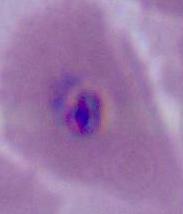

identification: Plasmodium
magnification: 400x or 1000x
modality: photomicrograph